Assess this cell for malaria.
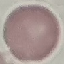
Uninfected.

Summary:
  - Capture: smartphone camera at the microscope eyepiece
  - Image type: cell patch, automatically extracted from a larger field of view and resized to 64 × 64 pixels
  - Stain: Giemsa
  - Preparation: thin blood smear